State which cell type is depicted.
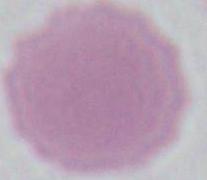
An erythrocyte.

magnification = 1000x
modality = photomicrograph